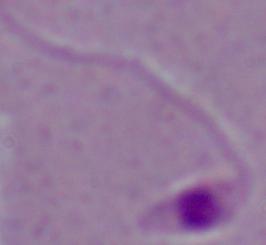
Captured at 1000x magnification. Photomicrograph. A Leishmania parasite is seen.